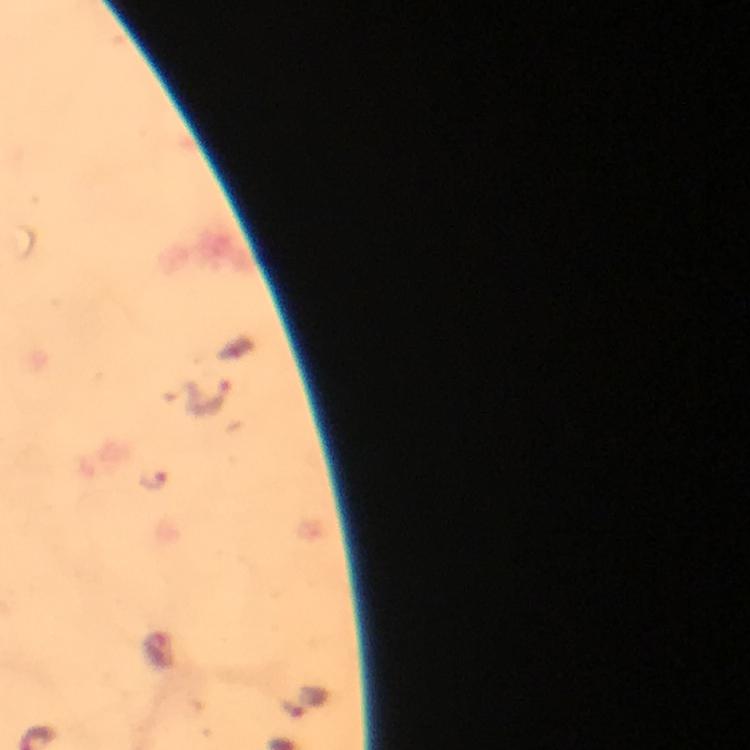
Approximate centers as (x, y) in pixels.
Summary:
  - Malaria parasite locations: (213, 397), (154, 482)
  - Cropped from: a single field of view
  - Immersion oil: applied
  - Capture: smartphone mounted on the microscope
  - Context: from a diagnostic examination for malaria
  - Stain: Giemsa
  - Image size: 750×750 pixels
  - Magnification: 100x
  - Preparation: thick blood film